Outline each blood parasite and name the species.
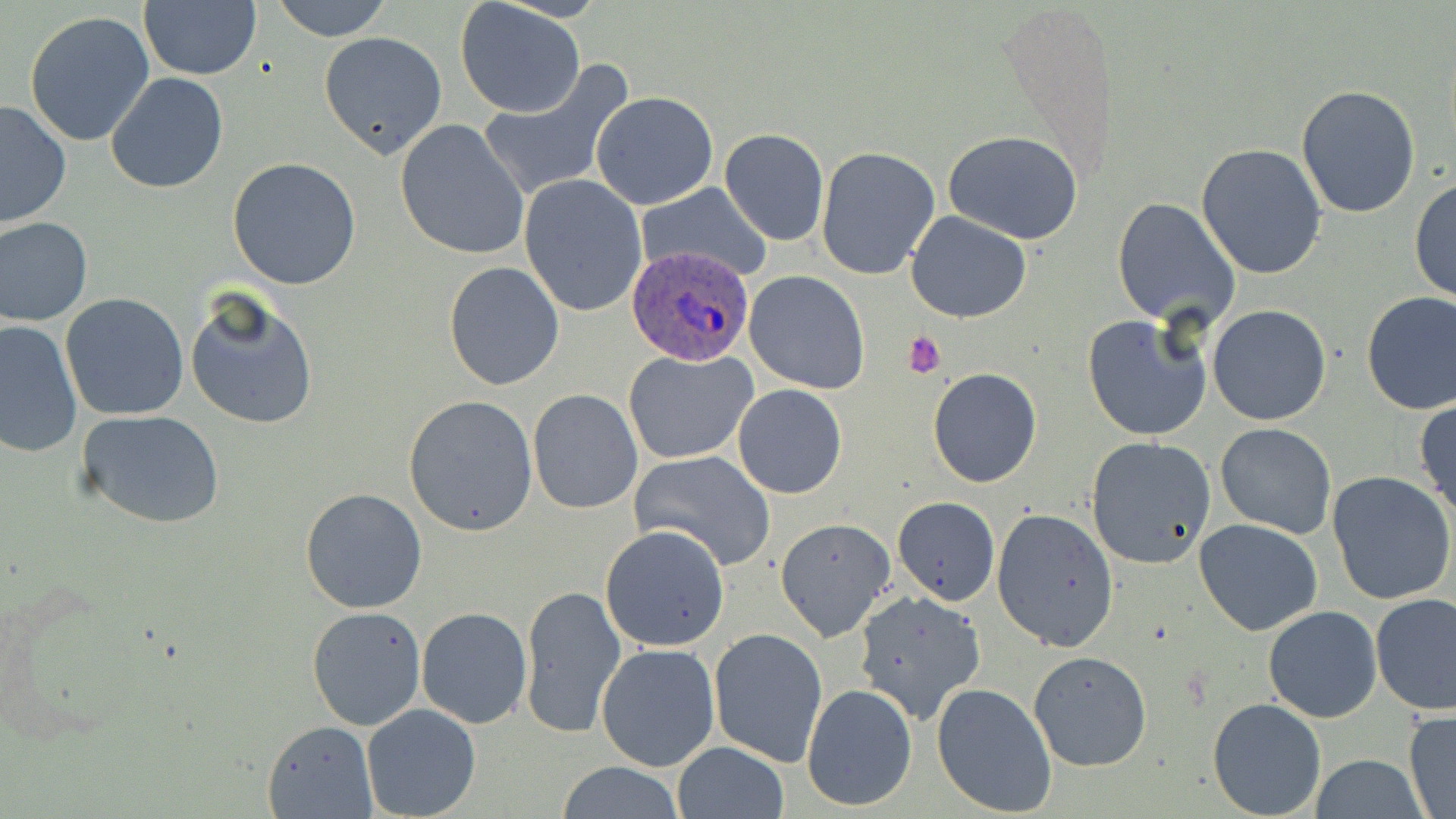
Approximate bounding boxes as (x1, y1, x2, y2) in pixels.
Plasmodium ovale-infected red blood cells: (626, 241, 760, 367).
No Plasmodium falciparum, Plasmodium malariae, Plasmodium vivax, Babesia divergens, or Trypanosoma brucei observed.

Platelet locations: (901, 330, 946, 377). Uninfected red blood cell locations: (270, 0, 394, 40), (456, 1, 586, 118), (138, 3, 262, 81), (25, 9, 156, 147), (319, 30, 449, 159), (475, 61, 636, 202), (106, 72, 229, 195), (1295, 83, 1422, 217), (591, 90, 718, 209), (0, 99, 74, 231), (394, 118, 531, 262), (720, 129, 829, 246), (942, 130, 1084, 242), (1195, 143, 1328, 281), (816, 146, 941, 280), (226, 157, 361, 290), (519, 174, 648, 317), (1410, 179, 1456, 304), (635, 180, 774, 282), (1112, 196, 1240, 328), (905, 211, 1031, 323), (0, 216, 94, 326), (443, 260, 565, 392), (744, 271, 871, 393), (184, 289, 319, 432), (1360, 291, 1456, 415), (61, 293, 190, 421), (1208, 304, 1330, 426), (1082, 313, 1213, 441), (1, 319, 82, 458), (623, 348, 757, 464), (927, 367, 1042, 487), (732, 384, 847, 499), (526, 388, 643, 513), (402, 394, 539, 537), (1414, 399, 1456, 518), (77, 409, 226, 529), (1215, 422, 1337, 539), (1085, 436, 1216, 569), (628, 449, 777, 573), (1328, 473, 1456, 607), (298, 487, 428, 614), (892, 497, 1000, 605), (991, 507, 1119, 654), (774, 517, 897, 644), (1194, 518, 1323, 636), (600, 524, 731, 650), (519, 583, 626, 737), (852, 589, 985, 723), (1371, 592, 1455, 713), (1262, 605, 1382, 722), (307, 606, 426, 731), (416, 607, 533, 729), (707, 626, 828, 766), (596, 643, 721, 773), (1027, 649, 1152, 772), (801, 682, 919, 812), (931, 682, 1059, 817), (1206, 698, 1328, 818), (361, 704, 483, 819), (1403, 708, 1456, 817), (262, 720, 377, 817), (672, 741, 790, 819), (1311, 754, 1427, 819), (555, 761, 686, 818). Slide-level diagnosis: Plasmodium ovale. Image is 1456×819 pixels. Light microscopy. May-Grünwald-Giemsa-stained preparation. Captured at 1000x magnification. Thin blood smear. Single field of view.